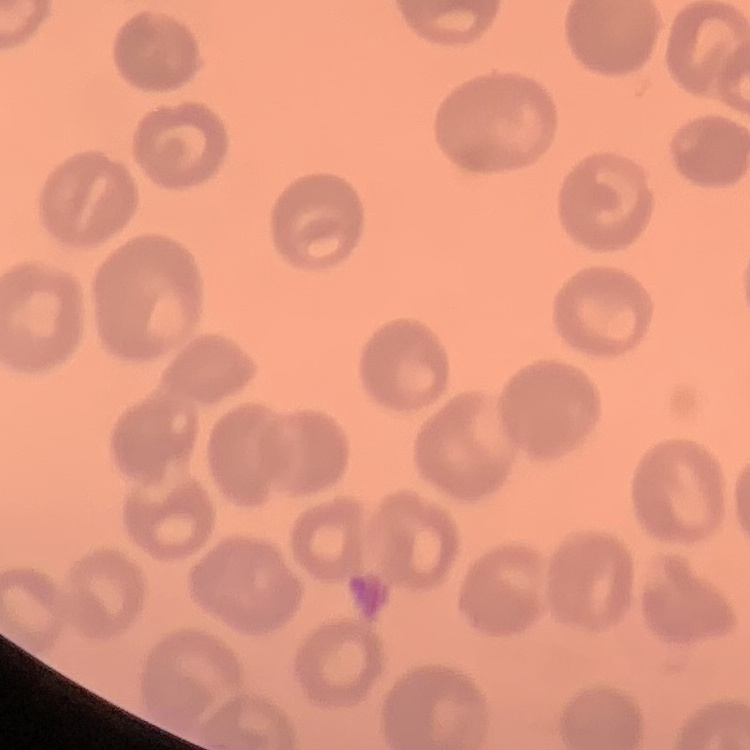
Summary:
  - Red blood cell morphology: no rouleaux formation
  - Stain: Field's or Giemsa
  - Image type: square crop of a larger photomicrograph
  - Preparation: thin peripheral smear